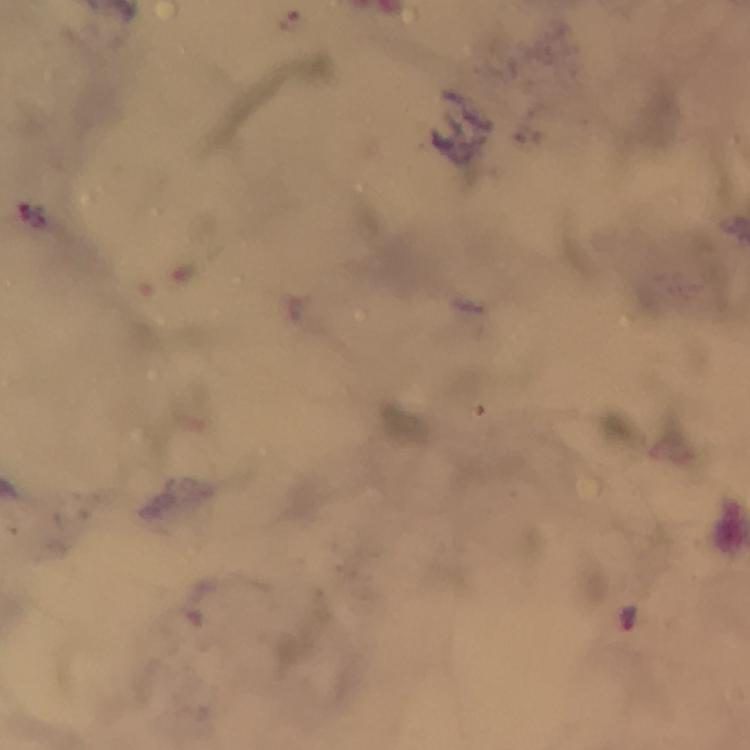
context = from a diagnostic examination for malaria
stain = Giemsa
malaria parasite locations = approximate object centers, in pixels from the top-left corner: (x=629, y=616)
magnification = 100x
cropped from = a single field of view
capture = smartphone photograph through a microscope
immersion oil = used
preparation = thick smear
image size = 750×750 pixels